Name the parasite shown.
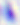

Toxoplasma gondii.

Captured at 400x magnification. Micrograph.